Assess the morphology of the erythrocytes.
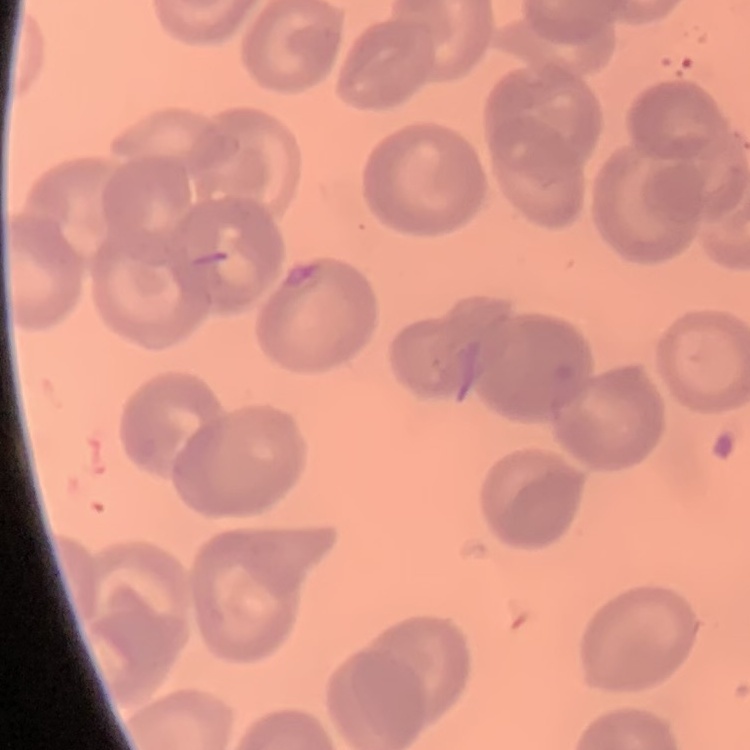
They show no rouleaux formation.

image type = square crop of a larger photomicrograph
stain = Field's or Giemsa
preparation = thin blood film